Locate every Plasmodium vivax-infected red blood cell.
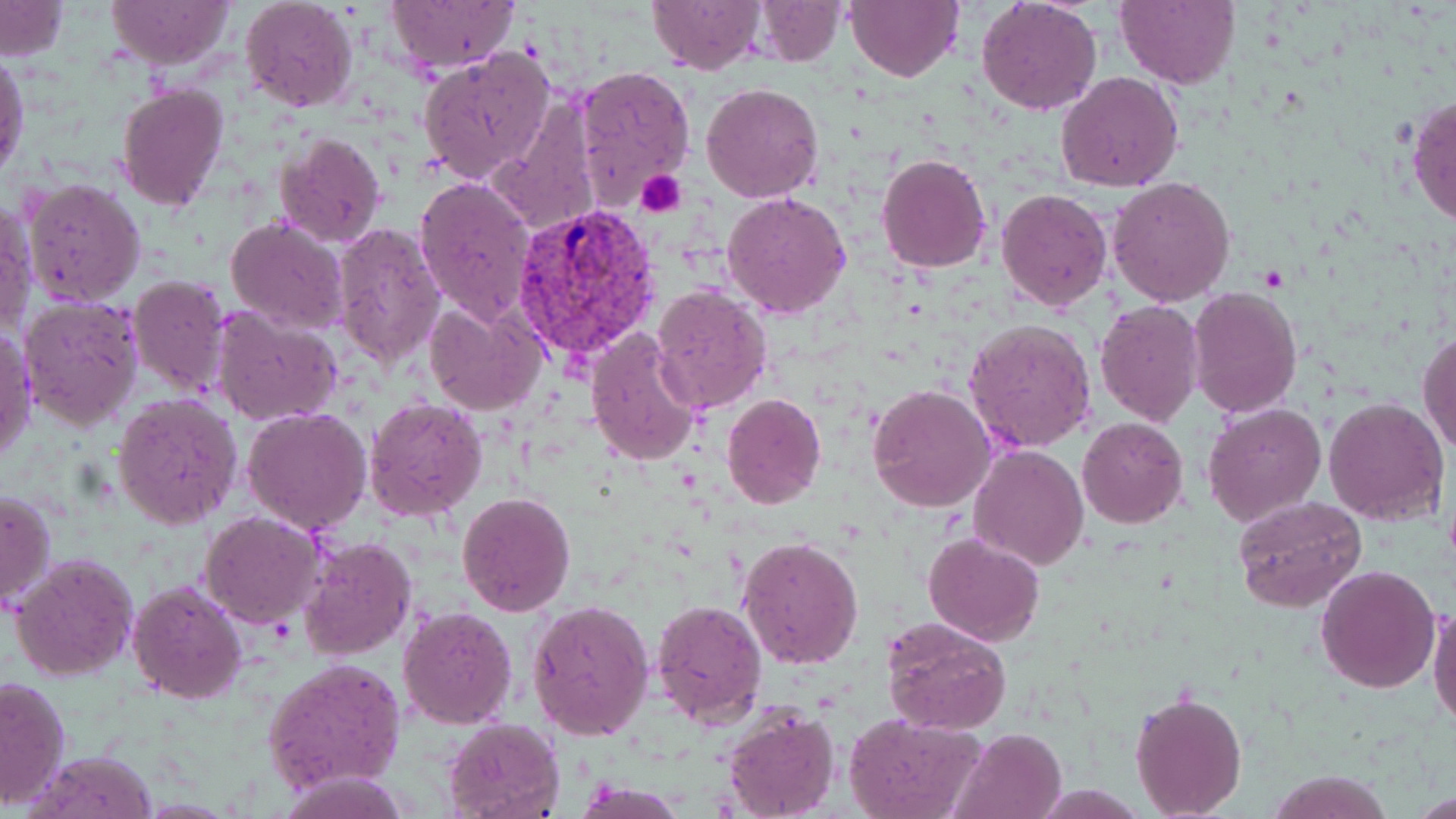

Approximate bounding boxes as (x1, y1, x2, y2) in pixels.
Plasmodium vivax-infected red blood cells: (509, 202, 663, 365).

slide_level_diagnosis: Plasmodium vivax
image_size: 1456×819 pixels
uninfected_red_blood_cell_locations: 'approximate bounding boxes as (x1, y1, x2, y2) in pixels: (104, 0, 234, 69), (386, 0, 518, 72), (647, 0, 764, 73), (748, 0, 849, 66), (845, 0, 963, 82), (976, 0, 1104, 115), (1114, 0, 1239, 89), (241, 1, 359, 112), (0, 2, 68, 59), (418, 47, 555, 184), (1, 51, 29, 181), (574, 64, 698, 204), (1056, 71, 1183, 192), (700, 81, 825, 204), (116, 84, 228, 211), (1407, 94, 1456, 227), (491, 98, 602, 236), (445, 108, 591, 298), (275, 131, 385, 248), (876, 153, 992, 274), (414, 174, 537, 323), (1108, 176, 1236, 305), (21, 178, 146, 305), (995, 187, 1112, 313), (723, 190, 852, 319), (0, 202, 37, 339), (225, 215, 348, 335), (330, 223, 445, 368), (128, 275, 231, 397), (652, 284, 772, 415), (1188, 286, 1302, 418), (19, 295, 144, 432), (424, 298, 546, 416), (1095, 299, 1205, 428), (212, 308, 343, 425), (965, 317, 1098, 452), (1, 327, 37, 463), (586, 329, 705, 468), (1417, 330, 1456, 456), (867, 384, 996, 511), (112, 392, 243, 530), (721, 394, 826, 510), (364, 395, 487, 520), (1323, 395, 1450, 527), (1203, 403, 1326, 529), (242, 406, 373, 536), (1078, 416, 1188, 530), (969, 445, 1088, 569), (1, 487, 55, 615), (457, 491, 577, 615), (1234, 494, 1367, 612), (200, 510, 327, 628), (924, 531, 1044, 647), (736, 533, 865, 671), (300, 536, 417, 659), (10, 553, 139, 682), (1315, 565, 1441, 694), (128, 580, 247, 702), (1428, 596, 1456, 729), (528, 599, 656, 742), (651, 600, 766, 726), (398, 606, 518, 728), (881, 615, 1014, 735), (265, 657, 405, 792), (0, 675, 70, 810), (1129, 689, 1248, 819), (719, 708, 839, 819), (844, 713, 988, 819), (444, 718, 564, 817), (952, 726, 1067, 819), (28, 751, 159, 819), (1269, 771, 1392, 817), (278, 772, 412, 817), (572, 782, 687, 818), (1414, 791, 1456, 817)'
platelet_locations: 'approximate bounding boxes as (x1, y1, x2, y2) in pixels: (635, 170, 687, 218)'
preparation: thin blood film
field_of_view: single
modality: light microscopy
magnification: 1000x
stain: May-Grünwald-Giemsa